Classify this cell by malaria status.
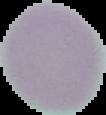
Uninfected.

The area outside the segmented cell region is set to black. From a thin blood film. Image is 106×115 pixels.